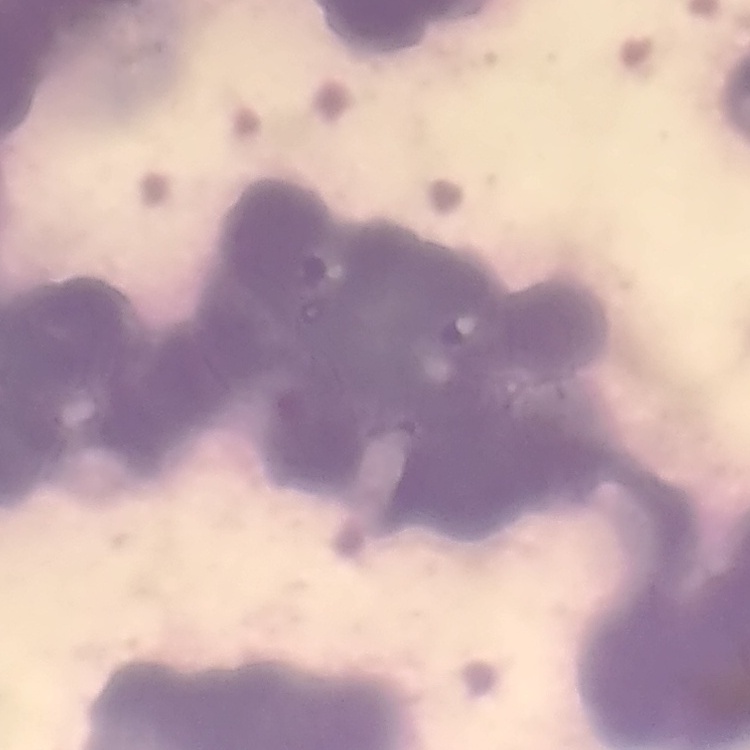

The erythrocytes exhibit rouleaux formation. Thin peripheral smear. One tile cut from a larger photomicrograph. Field's or Giemsa stain.